Identify the preparation type.
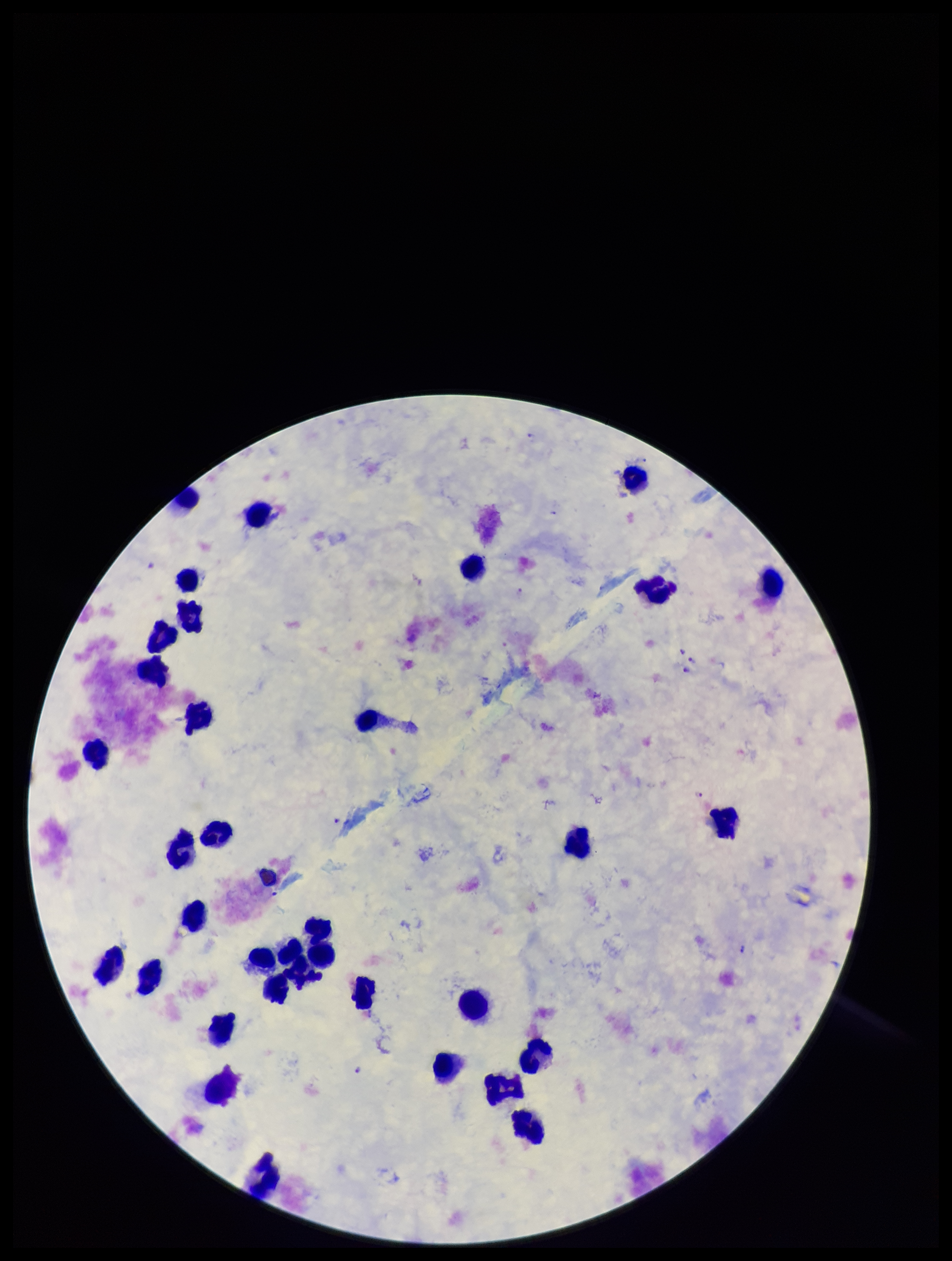

It is a thick blood smear.

Summary:
  - Leukocyte count: 34
  - Species reported for this patient: Plasmodium falciparum
  - Field of view: one from this slide
  - Patient malaria status: infected
  - Capture: smartphone photograph through the microscope eyepiece
  - Stain: Giemsa
  - Parasite count: 9
  - Image size: 952×1261 pixels
  - Plasmodium parasites: identified